Report the malaria status of this cell.
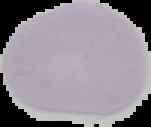
It is uninfected.

Image is 151×127 pixels. From a thin blood smear. Segmented cell region on a black background.